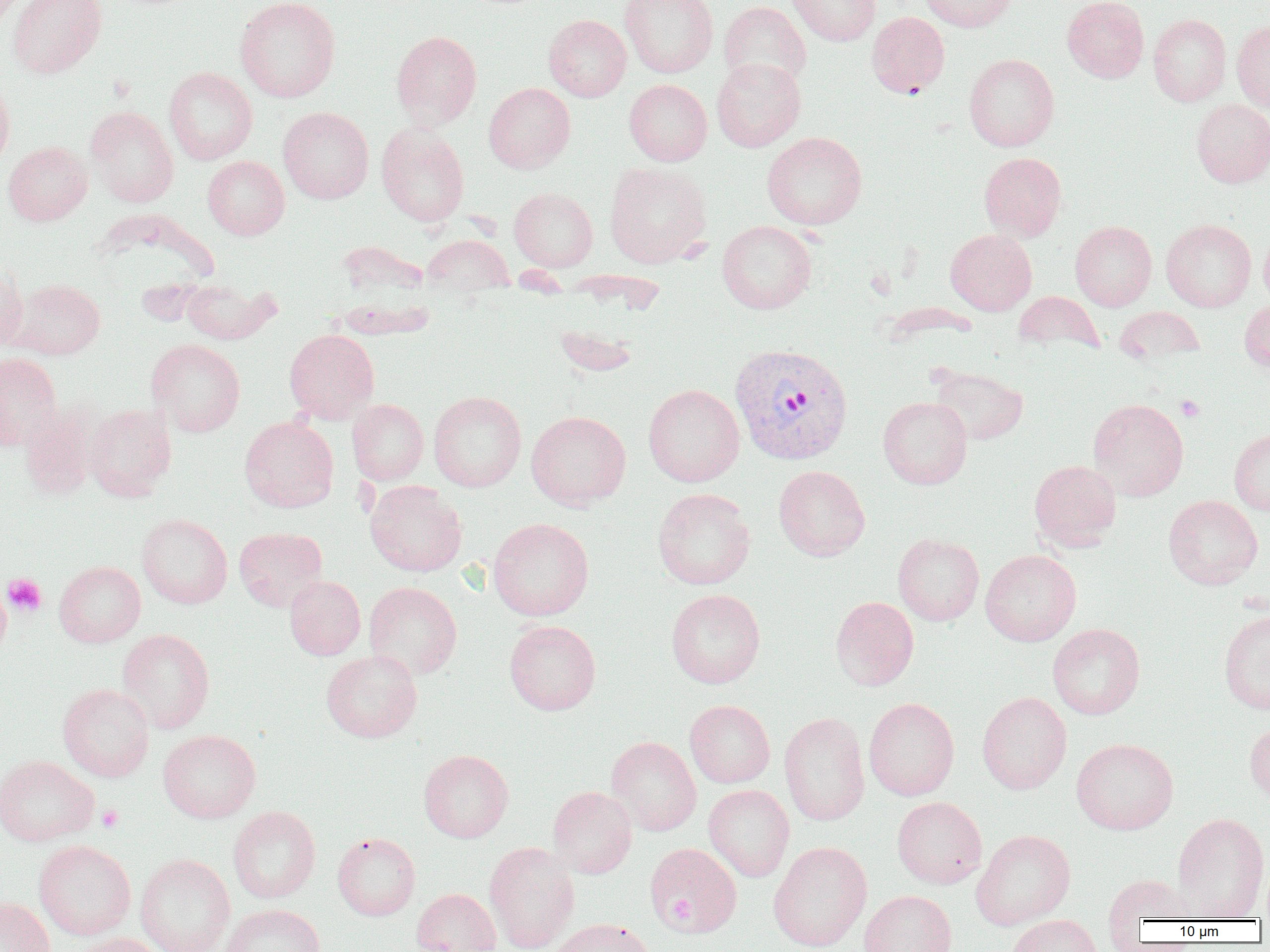

Approximate bounding boxes as named x1/y1/x2/y2 corners in pixels. Plasmodium vivax-infected red blood cell locations: (x1=729, y1=343, x2=853, y2=465). Platelet locations: (x1=1176, y1=395, x2=1205, y2=421), (x1=2, y1=573, x2=47, y2=617), (x1=97, y1=805, x2=124, y2=831), (x1=668, y1=897, x2=695, y2=923). Uninfected red blood cell locations: (x1=7, y1=0, x2=107, y2=79), (x1=234, y1=0, x2=341, y2=102), (x1=620, y1=0, x2=719, y2=78), (x1=786, y1=0, x2=880, y2=46), (x1=919, y1=0, x2=1018, y2=32), (x1=1062, y1=0, x2=1149, y2=82), (x1=718, y1=1, x2=811, y2=90), (x1=866, y1=11, x2=950, y2=98), (x1=544, y1=14, x2=631, y2=101), (x1=1148, y1=14, x2=1231, y2=106), (x1=1232, y1=19, x2=1270, y2=112), (x1=391, y1=30, x2=482, y2=129), (x1=964, y1=53, x2=1059, y2=151), (x1=711, y1=57, x2=806, y2=152), (x1=163, y1=67, x2=257, y2=165), (x1=0, y1=76, x2=15, y2=176), (x1=624, y1=79, x2=711, y2=166), (x1=484, y1=82, x2=575, y2=173), (x1=1191, y1=99, x2=1270, y2=187), (x1=85, y1=106, x2=179, y2=207), (x1=278, y1=107, x2=374, y2=204), (x1=376, y1=122, x2=469, y2=226), (x1=762, y1=131, x2=867, y2=229), (x1=3, y1=141, x2=92, y2=225), (x1=979, y1=152, x2=1067, y2=241), (x1=203, y1=156, x2=289, y2=239), (x1=604, y1=161, x2=712, y2=268), (x1=509, y1=187, x2=598, y2=271), (x1=1161, y1=218, x2=1256, y2=312), (x1=1070, y1=220, x2=1156, y2=311), (x1=717, y1=221, x2=816, y2=314), (x1=1259, y1=226, x2=1270, y2=309), (x1=946, y1=229, x2=1036, y2=315), (x1=422, y1=234, x2=514, y2=292), (x1=337, y1=240, x2=431, y2=299), (x1=0, y1=263, x2=28, y2=352), (x1=181, y1=278, x2=279, y2=344), (x1=9, y1=279, x2=105, y2=359), (x1=1014, y1=291, x2=1104, y2=355), (x1=1240, y1=297, x2=1270, y2=370), (x1=1114, y1=306, x2=1205, y2=364), (x1=553, y1=323, x2=641, y2=377), (x1=284, y1=329, x2=379, y2=423), (x1=146, y1=339, x2=246, y2=437), (x1=0, y1=353, x2=61, y2=450), (x1=930, y1=366, x2=1028, y2=445), (x1=643, y1=384, x2=744, y2=487), (x1=428, y1=391, x2=526, y2=492), (x1=878, y1=396, x2=972, y2=489), (x1=1088, y1=398, x2=1189, y2=501), (x1=347, y1=399, x2=429, y2=485), (x1=19, y1=403, x2=100, y2=500), (x1=84, y1=404, x2=176, y2=501), (x1=526, y1=411, x2=631, y2=510), (x1=239, y1=416, x2=339, y2=513), (x1=1229, y1=428, x2=1270, y2=515), (x1=1029, y1=460, x2=1121, y2=551), (x1=774, y1=465, x2=870, y2=561), (x1=365, y1=480, x2=467, y2=577), (x1=652, y1=488, x2=756, y2=590), (x1=1163, y1=495, x2=1262, y2=589), (x1=136, y1=514, x2=232, y2=609), (x1=488, y1=518, x2=594, y2=621), (x1=234, y1=527, x2=327, y2=611), (x1=893, y1=533, x2=984, y2=626), (x1=980, y1=549, x2=1081, y2=646), (x1=54, y1=561, x2=146, y2=647), (x1=284, y1=575, x2=366, y2=660), (x1=364, y1=581, x2=462, y2=680), (x1=0, y1=582, x2=10, y2=659), (x1=666, y1=588, x2=765, y2=688), (x1=830, y1=596, x2=919, y2=691), (x1=1218, y1=609, x2=1270, y2=714), (x1=504, y1=620, x2=601, y2=715), (x1=1047, y1=623, x2=1145, y2=719), (x1=117, y1=629, x2=215, y2=733), (x1=321, y1=650, x2=422, y2=743), (x1=57, y1=683, x2=155, y2=781), (x1=977, y1=691, x2=1072, y2=795), (x1=863, y1=698, x2=959, y2=800), (x1=685, y1=700, x2=775, y2=788), (x1=779, y1=712, x2=870, y2=826), (x1=1244, y1=719, x2=1270, y2=803), (x1=158, y1=729, x2=260, y2=823), (x1=606, y1=736, x2=702, y2=836), (x1=1071, y1=738, x2=1178, y2=835), (x1=418, y1=749, x2=514, y2=842), (x1=0, y1=755, x2=98, y2=846), (x1=704, y1=784, x2=794, y2=882), (x1=547, y1=786, x2=637, y2=878), (x1=892, y1=796, x2=987, y2=889), (x1=228, y1=806, x2=320, y2=903), (x1=1172, y1=812, x2=1270, y2=920), (x1=971, y1=829, x2=1075, y2=930), (x1=332, y1=832, x2=420, y2=920), (x1=33, y1=840, x2=136, y2=941), (x1=768, y1=841, x2=871, y2=952), (x1=484, y1=842, x2=580, y2=952), (x1=648, y1=845, x2=743, y2=937), (x1=135, y1=854, x2=235, y2=952), (x1=1101, y1=872, x2=1198, y2=933), (x1=411, y1=888, x2=501, y2=952), (x1=859, y1=890, x2=957, y2=952), (x1=0, y1=896, x2=54, y2=952), (x1=221, y1=904, x2=326, y2=952), (x1=1006, y1=914, x2=1102, y2=952), (x1=550, y1=918, x2=655, y2=952), (x1=68, y1=932, x2=168, y2=952). Slide-level diagnosis: Plasmodium vivax. Light microscopy. Image is 1270×952 pixels. Thin blood film. Single field of view. Captured at 1000x magnification.